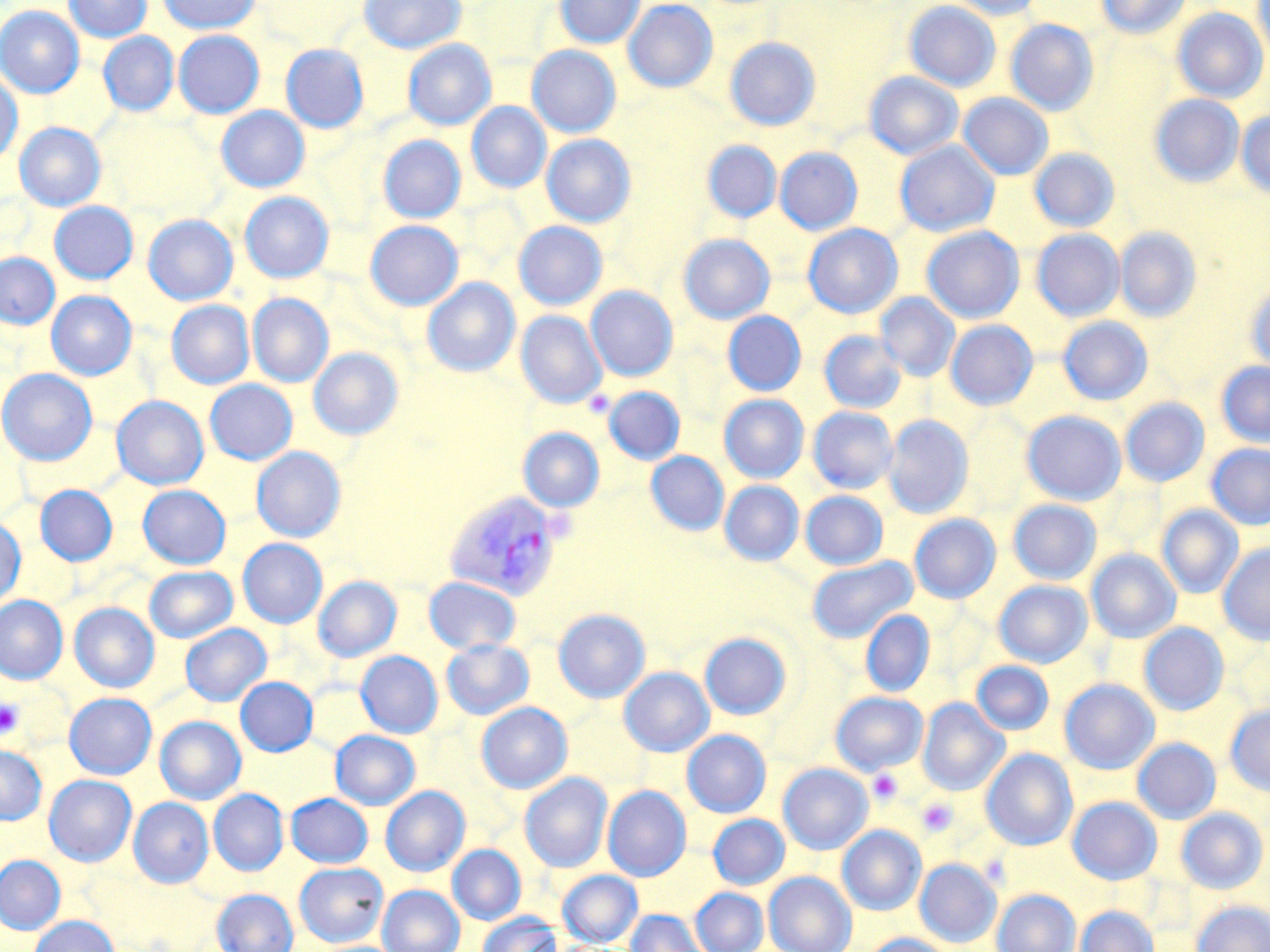
Approximate bounding boxes as [x1, y1, x2, y2] in pixels. Platelet locations: [0, 698, 24, 738], [867, 769, 904, 804], [916, 798, 958, 836]. Plasmodium vivax-infected red blood cell locations: [444, 490, 564, 601]. Uninfected red blood cell locations: [63, 0, 151, 42], [158, 0, 262, 34], [359, 0, 465, 54], [555, 0, 645, 48], [623, 0, 718, 92], [947, 0, 1045, 19], [1096, 0, 1190, 38], [904, 1, 1001, 91], [1253, 1, 1270, 62], [0, 6, 84, 97], [1172, 8, 1268, 102], [1005, 19, 1099, 115], [173, 30, 264, 118], [98, 32, 178, 116], [724, 37, 820, 130], [403, 39, 496, 130], [280, 44, 368, 133], [526, 45, 621, 137], [0, 71, 23, 165], [865, 72, 963, 159], [958, 93, 1053, 180], [1150, 94, 1244, 187], [466, 102, 551, 193], [216, 106, 309, 192], [1236, 110, 1270, 198], [14, 122, 106, 211], [541, 134, 636, 227], [378, 135, 465, 223], [702, 140, 781, 223], [895, 141, 1000, 236], [775, 148, 863, 235], [1030, 148, 1120, 232], [245, 191, 332, 385], [240, 192, 333, 282], [49, 201, 138, 284], [142, 215, 238, 305], [364, 220, 463, 310], [513, 221, 607, 309], [803, 223, 903, 318], [921, 226, 1024, 322], [1115, 227, 1202, 322], [1031, 229, 1124, 321], [678, 234, 775, 324], [0, 252, 60, 329], [422, 278, 520, 377], [1245, 282, 1270, 372], [586, 286, 678, 381], [46, 291, 137, 380], [875, 293, 960, 381], [248, 294, 334, 387], [166, 300, 254, 389], [516, 311, 607, 408], [723, 311, 806, 396], [1058, 316, 1153, 405], [946, 320, 1038, 410], [819, 330, 907, 413], [309, 348, 403, 440], [1216, 361, 1270, 447], [0, 369, 97, 465], [204, 379, 297, 464], [603, 387, 684, 464], [719, 394, 809, 482], [111, 395, 208, 490], [1120, 398, 1209, 486], [808, 407, 898, 493], [1022, 410, 1126, 505], [883, 415, 973, 518], [518, 427, 604, 512], [1206, 444, 1270, 529], [251, 447, 346, 542], [646, 451, 728, 535], [720, 481, 803, 565], [35, 485, 118, 566], [138, 485, 231, 569], [800, 490, 888, 569], [1008, 499, 1101, 584], [1157, 505, 1244, 598], [909, 514, 1000, 603], [0, 518, 26, 610], [238, 538, 327, 628], [1218, 543, 1270, 644], [1087, 549, 1180, 643], [807, 556, 918, 643], [144, 566, 237, 642], [313, 576, 401, 661], [424, 577, 521, 654], [994, 580, 1092, 667], [0, 595, 68, 683], [69, 602, 159, 692], [553, 609, 650, 702], [860, 610, 934, 697], [180, 623, 271, 706], [1139, 623, 1228, 715], [700, 632, 791, 720], [441, 639, 534, 720], [355, 651, 443, 738], [971, 661, 1054, 735], [619, 667, 714, 756], [235, 677, 318, 756], [1060, 679, 1159, 774], [64, 692, 156, 779], [830, 692, 927, 775], [918, 699, 1008, 796], [477, 702, 572, 793], [1225, 705, 1270, 795], [155, 716, 246, 804], [330, 730, 420, 809], [682, 730, 771, 817], [1132, 738, 1220, 823], [0, 745, 47, 825], [981, 749, 1077, 850], [778, 764, 872, 854], [520, 773, 612, 872], [44, 775, 136, 866], [381, 786, 469, 876], [603, 786, 691, 880], [209, 789, 288, 875], [286, 793, 373, 868], [129, 797, 213, 887], [1067, 797, 1161, 884], [1176, 807, 1268, 893], [708, 814, 789, 889], [837, 826, 925, 915], [447, 844, 526, 924], [0, 855, 65, 934], [915, 859, 1001, 946], [294, 862, 388, 946], [557, 870, 643, 946], [764, 872, 856, 952], [377, 885, 465, 952], [690, 887, 768, 952], [212, 888, 299, 952], [992, 889, 1080, 952], [1191, 901, 1270, 952], [1075, 906, 1159, 952], [625, 910, 706, 952], [477, 913, 562, 952], [29, 915, 119, 952], [863, 934, 955, 952]. Slide-level diagnosis: Plasmodium vivax. Thin blood smear. Light microscopy. Image is 1270×952 pixels. 1000x magnification. May-Grünwald-Giemsa-stained preparation. One field of a larger specimen.